Assess this cell for malaria.
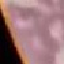
Uninfected.

{
  "preparation": "thin smear",
  "capture": "smartphone through the microscope eyepiece",
  "image_type": "cell patch, automatically extracted from a larger field of view and resized to 64 × 64 pixels",
  "stain": "Giemsa"
}